Comment on the morphology of the red blood cells.
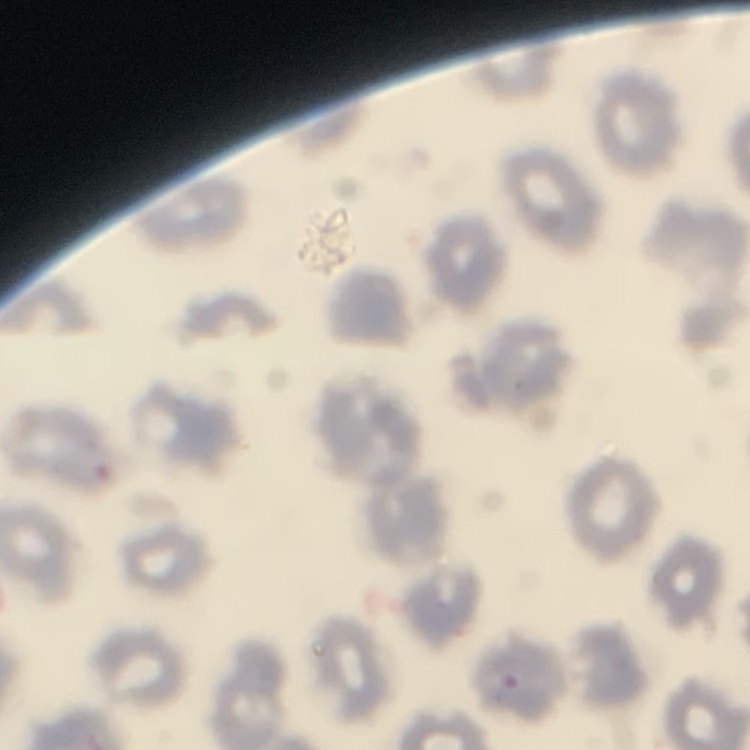
No rouleaux formation.

stain = Field's or Giemsa
preparation = thin blood smear
image type = one tile cut from a larger photomicrograph